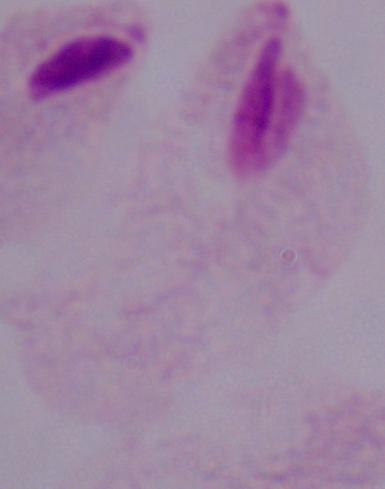
Summary:
  - Magnification: 1000x
  - Modality: micrograph
  - Identification: trichomonad